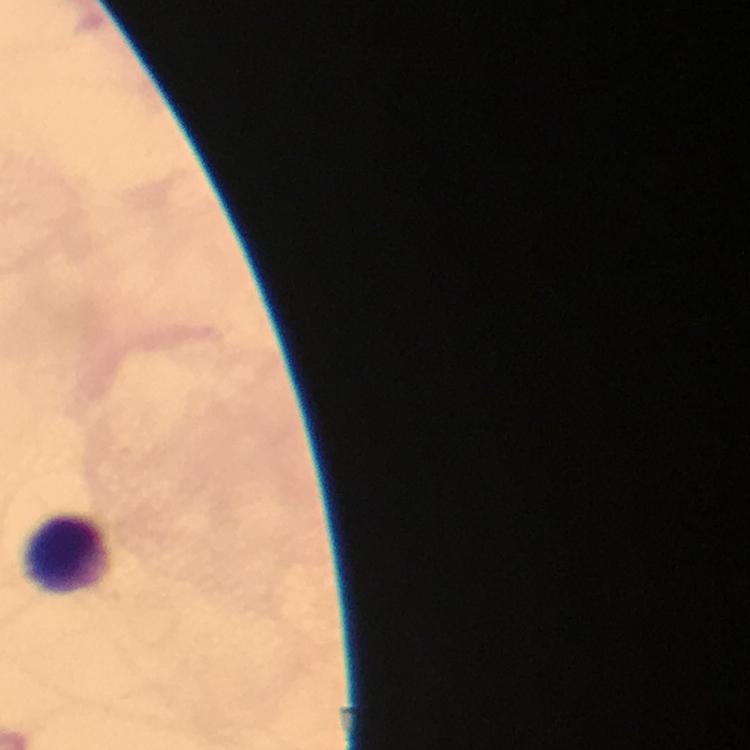

Approximate centers as [x, y] in pixels.
Summary:
  - Leukocyte locations: [65, 552]
  - Immersion oil: used
  - Stain: Giemsa
  - Context: from a malaria diagnostic workup
  - Capture: smartphone mounted on the microscope
  - Image size: 750×750 pixels
  - Cropped from: one field of view
  - Preparation: thick blood smear
  - Malaria parasites: none detected
  - Magnification: 100x